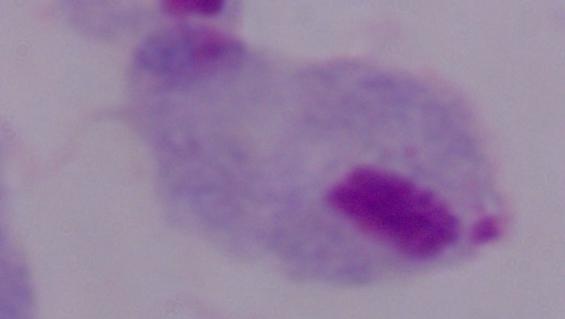
identification = trichomonad
magnification = 1000x
modality = micrograph